Comment on the morphology of the red blood cells.
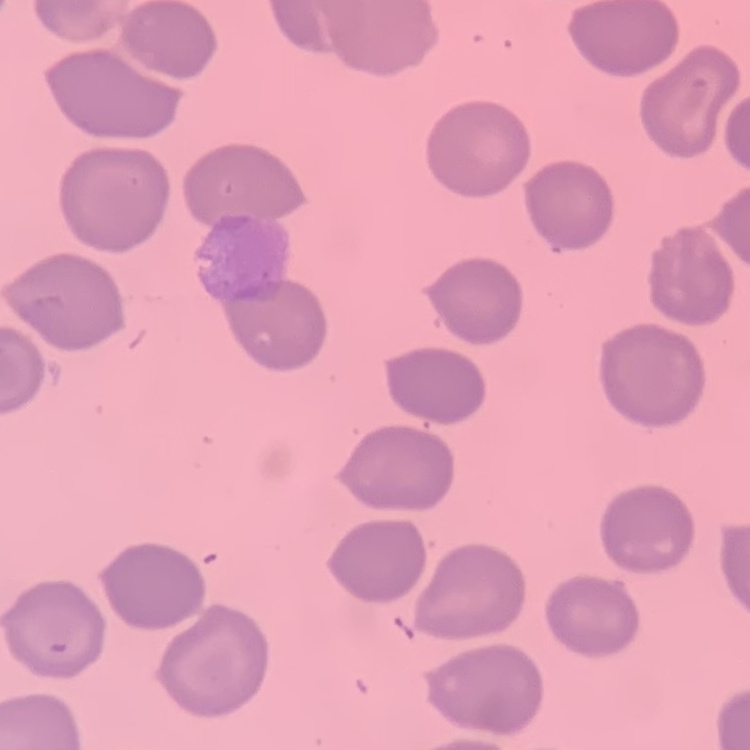
They show no rouleaux formation.

Stained with either Field's or Giemsa. One tile cut from a larger photomicrograph. Thin blood smear.